Describe the morphology of the erythrocytes.
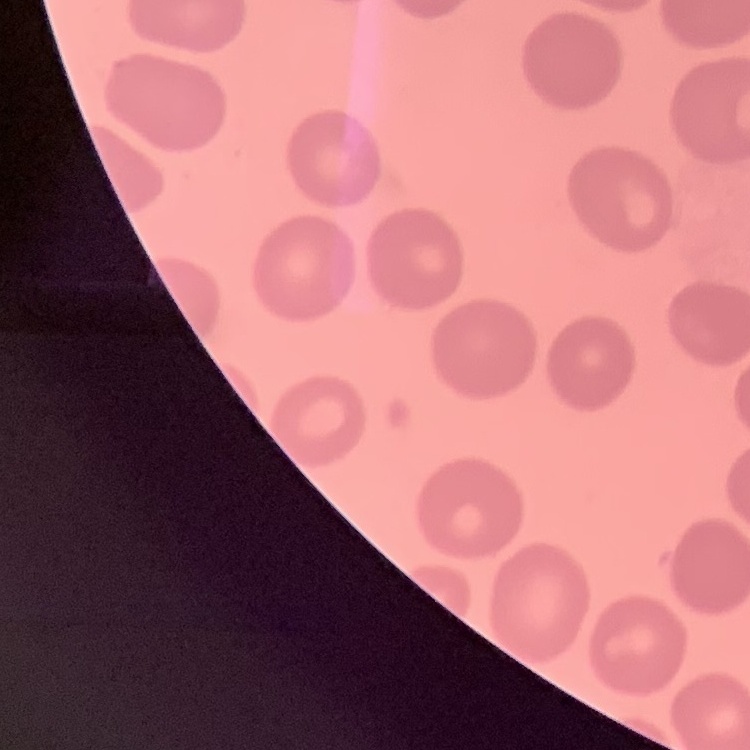
No rouleaux formation.

Stained with either Field's or Giemsa. Thin peripheral smear. One tile cut from a larger photomicrograph.